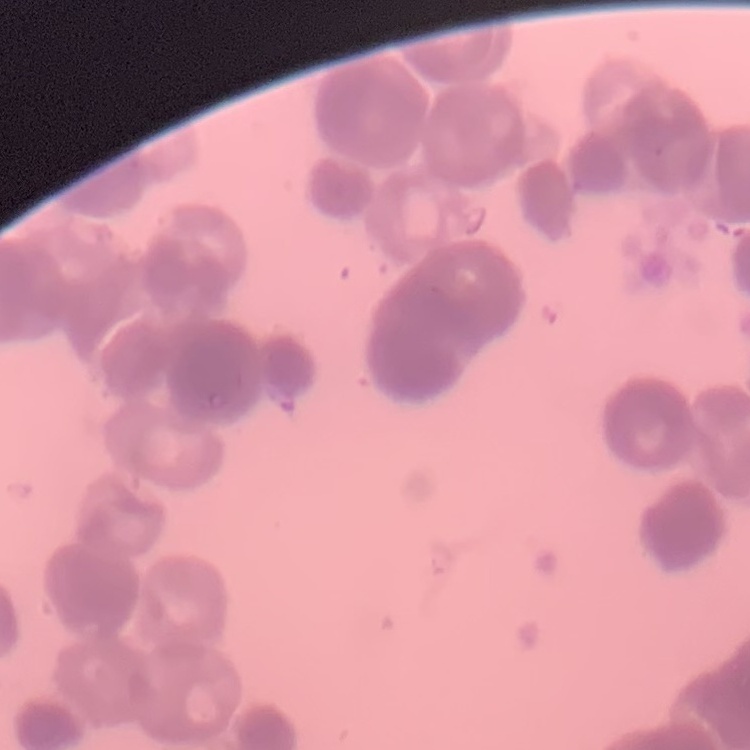 The erythrocytes exhibit rouleaux formation. Thin blood smear. Square crop of a larger photomicrograph. Stained with either Field's or Giemsa.